Give the position of each Plasmodium falciparum parasite with its life-cycle stage, each leukocyte, and any debris.
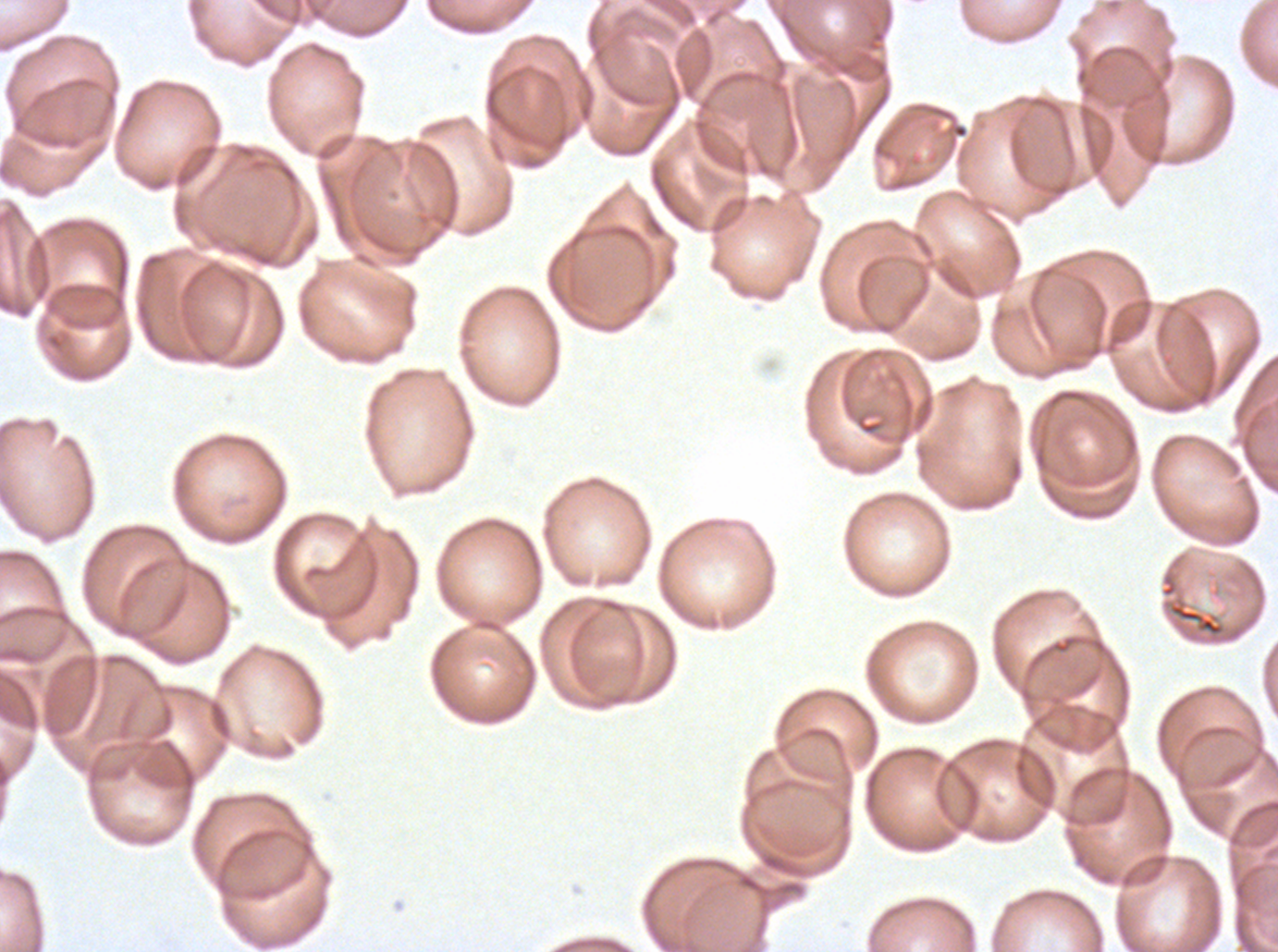

Approximate bounding boxes as {x1, y1, x2, y2} in pixels.
Debris: {1168, 602, 1225, 637}.
No rings, late-ring/early-trophozoite forms, mid trophozoites, late trophozoites, early schizonts, late schizonts, segmenters, gametocytes, or leukocytes observed.

{
  "field_of_view": "one sub-image of a larger composite",
  "stain": "Giemsa",
  "specimen": "ex-vivo Plasmodium falciparum culture from a patient in The Gambia, grown for 24 to 48 hours",
  "preparation": "thin blood film",
  "image_size": "1278×952 pixels"
}